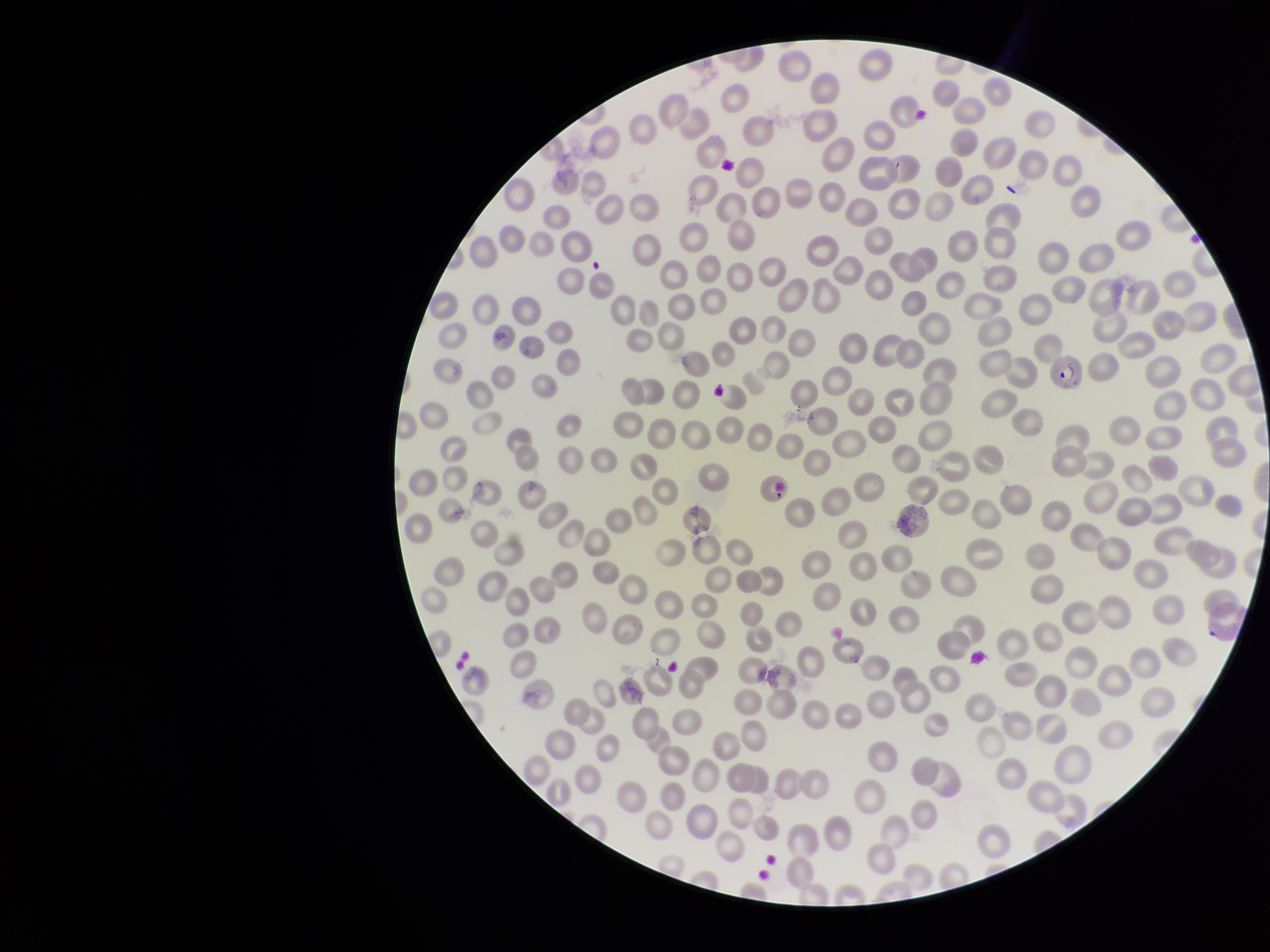
Summary:
  - Stain: Giemsa
  - Field of view: one from this slide
  - Parasitized red blood cells: detected
  - Parasitized red blood cell count: 1
  - Patient malaria status: positive
  - Capture: smartphone photograph through the microscope eyepiece
  - Preparation: thin blood smear
  - Red blood cell count: 286
  - Species reported for this patient: Plasmodium vivax
  - Image size: 1270×952 pixels